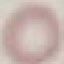 Malaria status: uninfected. Photographed with a smartphone camera at the microscope eyepiece. Giemsa stain. Thin blood film. Cell patch, automatically extracted from a larger field of view and resized to 64 × 64 pixels.